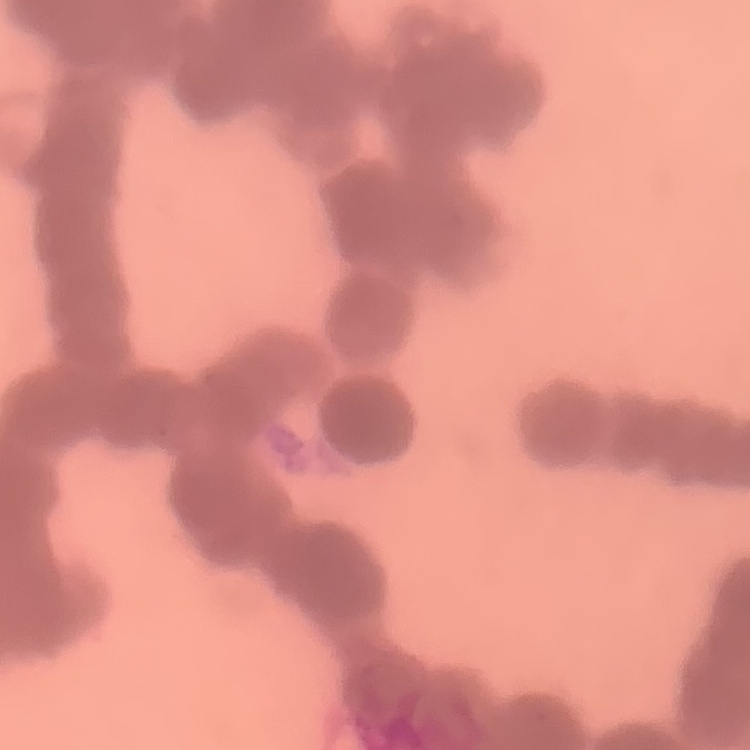

Summary:
  - Erythrocyte morphology: rouleaux formation
  - Stain: Field's or Giemsa
  - Image type: square crop of a larger photomicrograph
  - Preparation: thin blood film